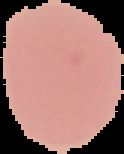

preparation = thin blood smear
image type = segmented cell region on a black background
image size = 124×154 pixels
result = no Plasmodium parasites seen